State which parasite is depicted.
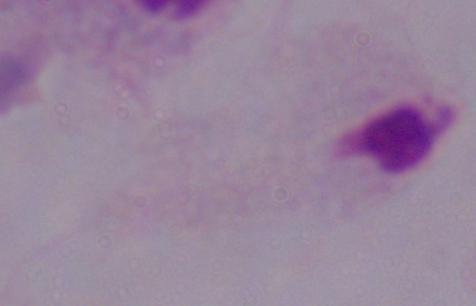
This is a trichomonad.

Summary:
  - Modality: micrograph
  - Magnification: 1000x